State the blood parasite species.
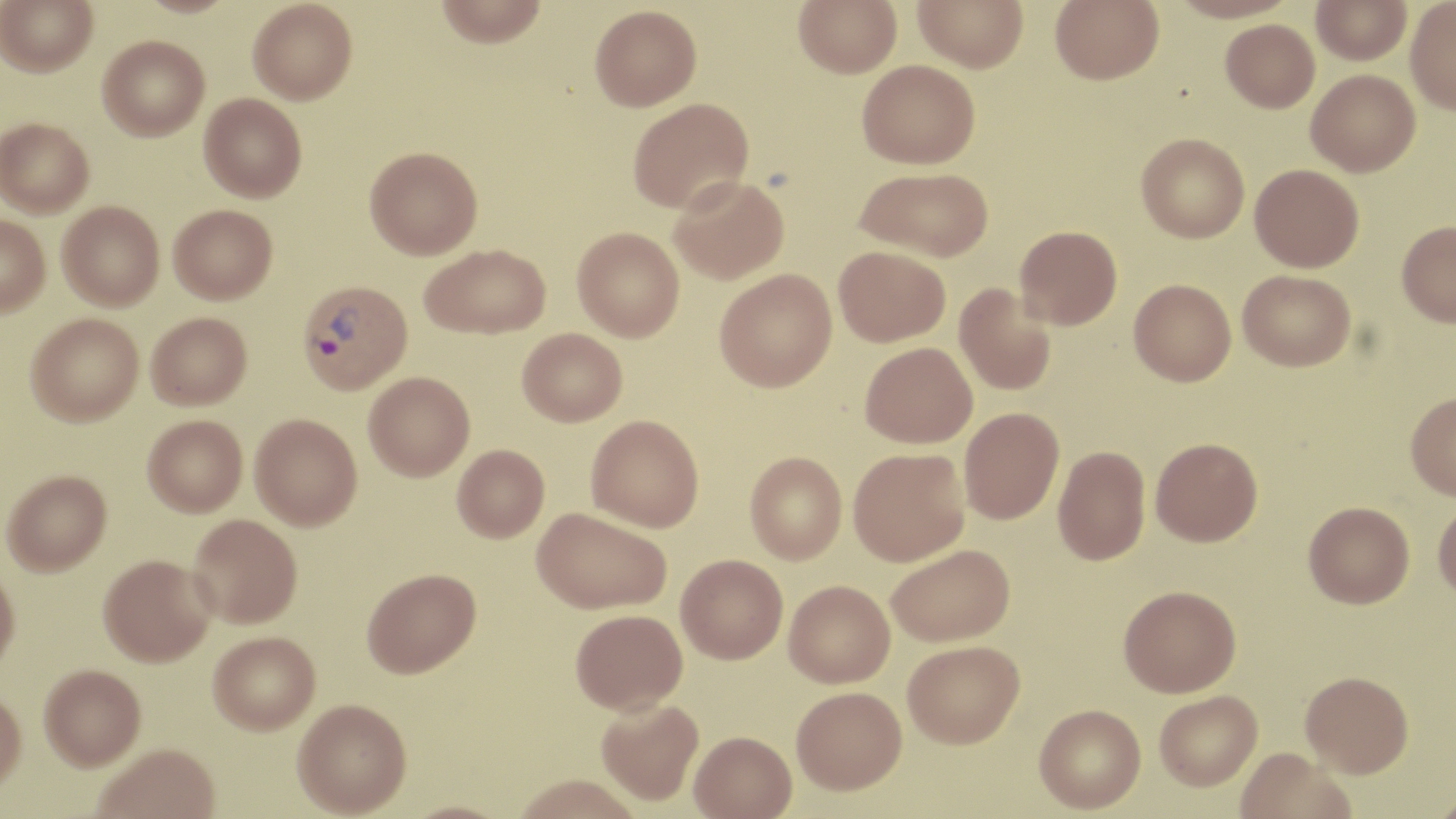

Plasmodium vivax.

Approximate bounding boxes as (x1,y1)-(x2,y2) corner pairs in pixels. Plasmodium vivax-infected red blood cell locations: (296,279)-(412,394). Uninfected red blood cell locations: (1,0)-(98,76), (248,0)-(357,104), (435,0)-(547,47), (794,0)-(902,77), (913,0)-(1028,72), (1050,0)-(1164,84), (1311,1)-(1411,64), (1405,1)-(1456,114), (589,5)-(702,111), (1220,18)-(1320,112), (98,35)-(209,141), (857,59)-(979,168), (1306,69)-(1420,176), (199,92)-(307,202), (627,98)-(754,213), (0,118)-(94,217), (1136,133)-(1249,243), (365,146)-(483,259), (1250,163)-(1364,272), (855,166)-(994,262), (668,175)-(789,284), (57,201)-(164,310), (169,204)-(277,304), (0,213)-(50,316), (1396,221)-(1456,327), (1015,225)-(1122,329), (572,226)-(684,341), (420,243)-(551,338), (834,245)-(950,346), (714,268)-(837,392), (1238,270)-(1356,371), (1129,279)-(1236,386), (954,283)-(1056,396), (26,312)-(144,425), (146,312)-(252,410), (517,328)-(627,426), (860,342)-(977,448), (364,371)-(475,481), (1405,391)-(1456,500), (959,407)-(1064,524), (250,413)-(362,530), (586,414)-(704,532), (142,415)-(247,516), (1151,437)-(1263,546), (452,444)-(550,541), (1053,445)-(1150,565), (848,447)-(970,566), (745,451)-(847,564), (2,469)-(112,575), (1433,499)-(1456,602), (1303,501)-(1414,608), (532,507)-(671,614), (188,514)-(302,628), (885,544)-(1016,647), (98,554)-(216,666), (676,554)-(788,663), (362,567)-(481,677), (0,568)-(20,677), (783,580)-(895,688), (1118,585)-(1241,697), (570,608)-(687,715), (208,631)-(320,735), (902,640)-(1025,748), (39,665)-(146,772), (1300,671)-(1414,777), (791,686)-(907,794), (1154,690)-(1262,790), (0,691)-(27,796), (595,697)-(704,806), (293,698)-(412,817), (1034,704)-(1146,813), (689,730)-(797,819), (93,745)-(220,819), (1236,748)-(1355,819), (511,774)-(643,819), (1432,788)-(1456,819), (398,800)-(515,819). One field of a larger specimen. Light microscopy. Thin blood smear. May-Grünwald-Giemsa stain. Captured at 1000x magnification. Image is 1456×819 pixels.